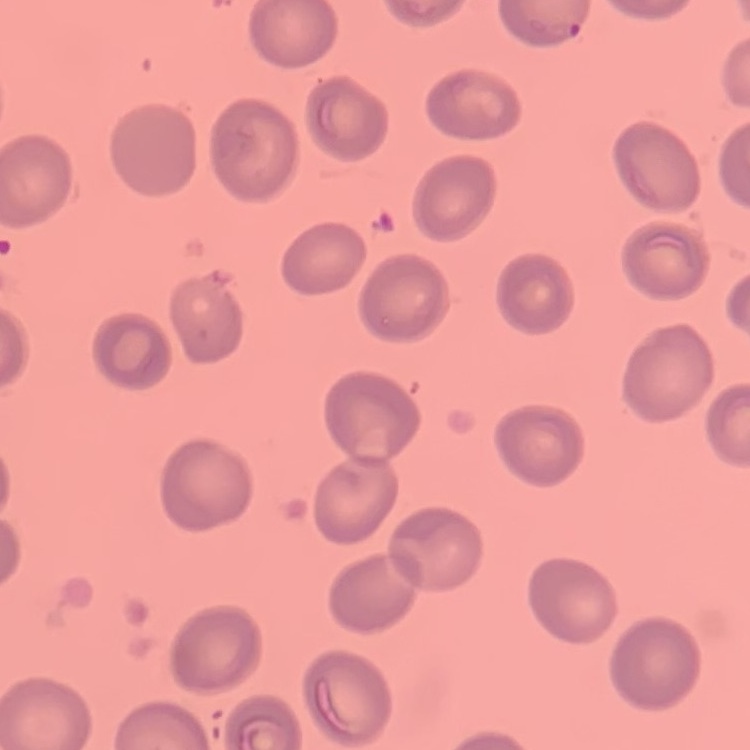

The red blood cells show no rouleaux formation. Thin blood film. One tile cut from a larger photomicrograph. Field's or Giemsa stain.